Give the position of every leukocyte visible.
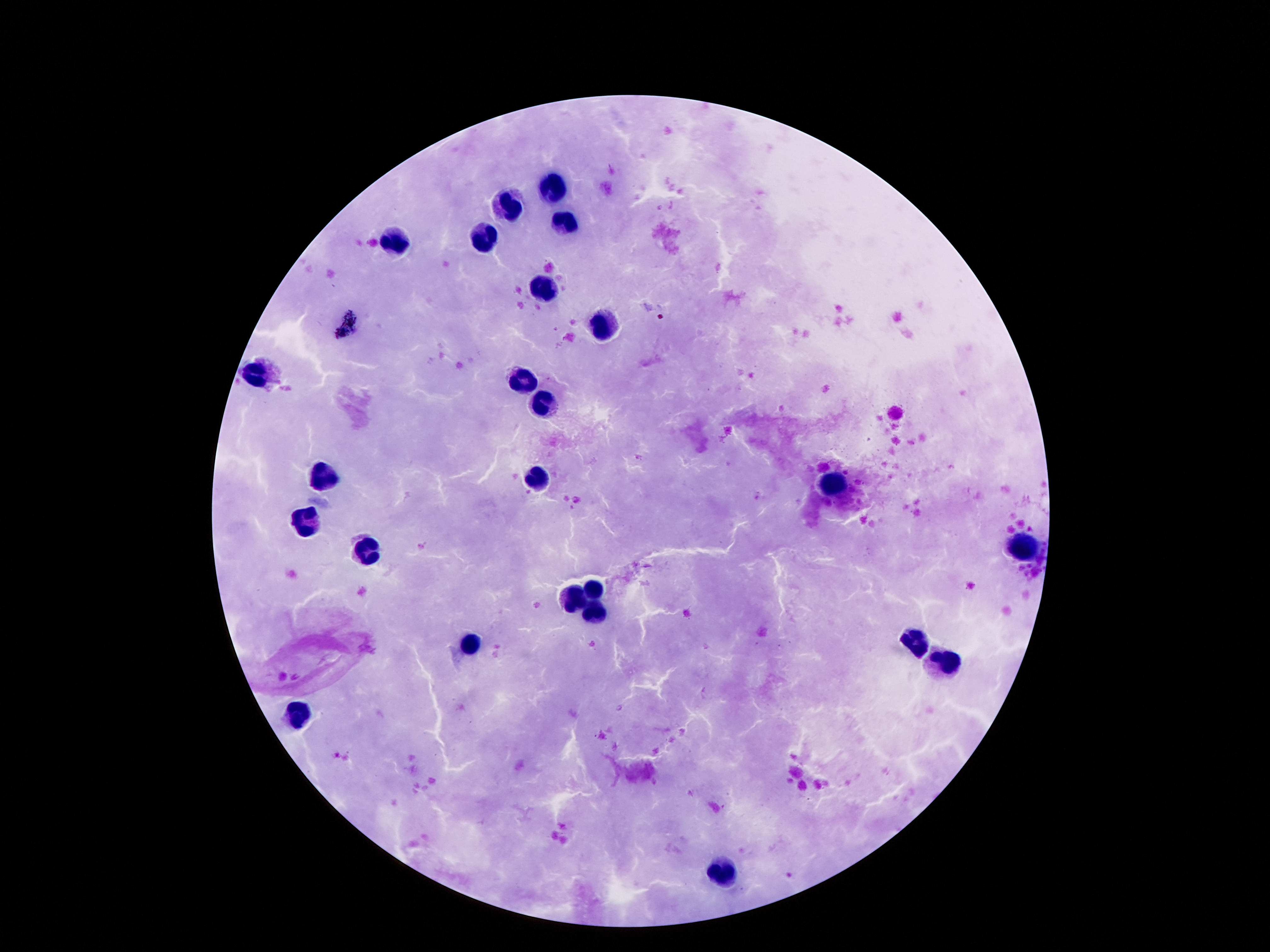
Approximate object centers, in pixels from the top-left corner.
Leukocytes: (x=554, y=191), (x=509, y=208), (x=561, y=227), (x=396, y=240), (x=480, y=242), (x=545, y=289), (x=600, y=326), (x=261, y=373), (x=518, y=379), (x=547, y=405), (x=539, y=477), (x=322, y=479), (x=832, y=485), (x=305, y=523), (x=369, y=547), (x=1024, y=547), (x=595, y=589), (x=575, y=596), (x=595, y=611), (x=472, y=644), (x=917, y=644), (x=948, y=663), (x=300, y=713), (x=727, y=869).

Summary:
  - Field of view: single
  - Image size: 1270×952 pixels
  - Magnification: 100x
  - Preparation: thick peripheral-blood smear
  - Patient malaria status: not infected
  - Capture: smartphone camera through the microscope eyepiece
  - Stain: Giemsa